Identify the blood parasite species.
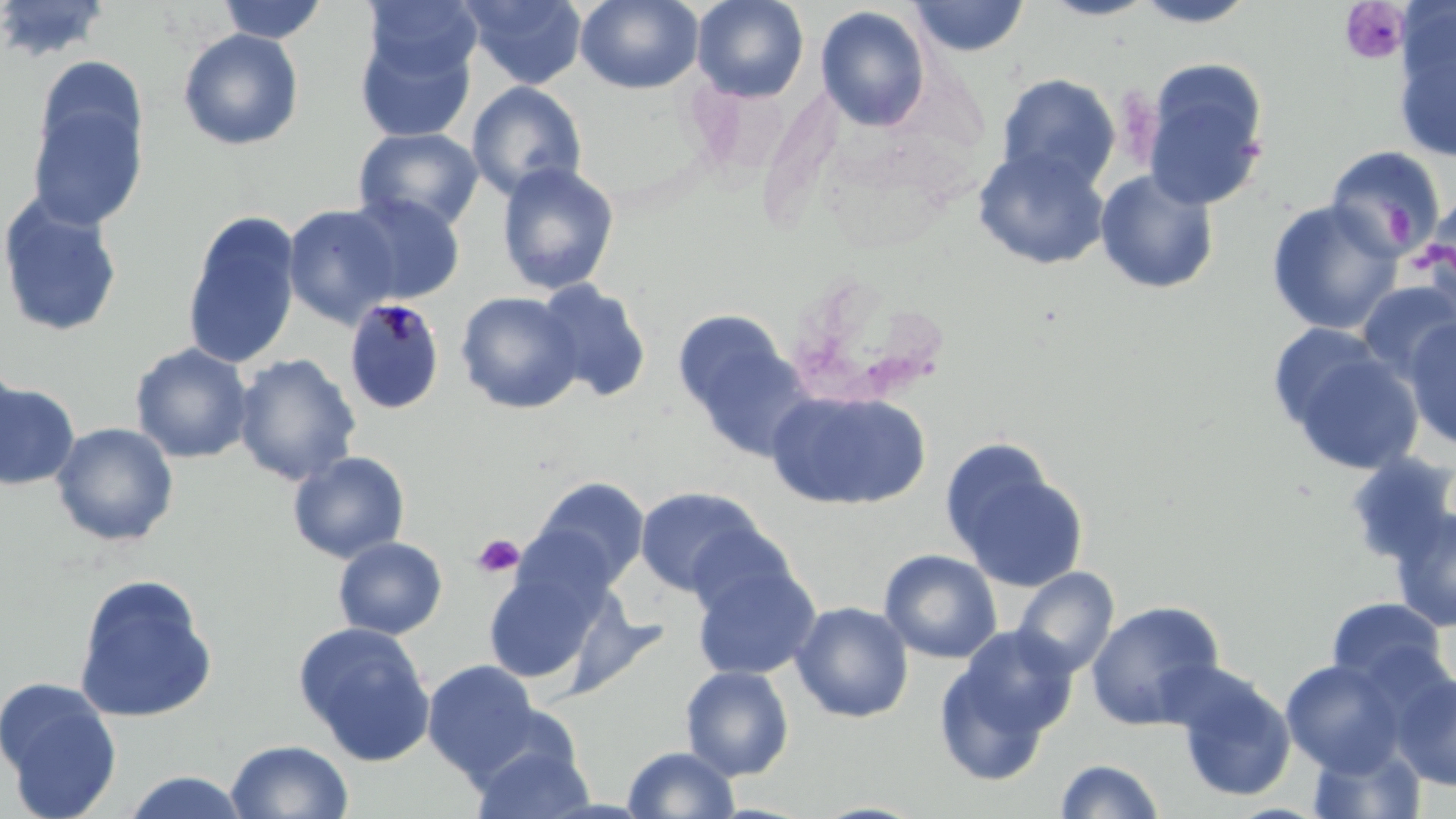
Plasmodium malariae.

Summary:
  - Coordinate format: approximate bounding boxes as (x1, y1, x2, y2) in pixels
  - Uninfected red blood cell locations: (0, 0, 112, 64), (217, 0, 328, 44), (461, 0, 587, 90), (575, 0, 703, 94), (692, 0, 810, 102), (1039, 0, 1158, 21), (1129, 0, 1263, 28), (363, 1, 482, 85), (909, 1, 1029, 57), (815, 5, 931, 132), (1390, 9, 1456, 163), (353, 20, 478, 143), (177, 28, 304, 151), (34, 55, 149, 168), (1141, 58, 1272, 211), (996, 73, 1121, 193), (466, 81, 587, 202), (27, 96, 147, 231), (353, 127, 483, 233), (973, 146, 1110, 270), (1324, 146, 1445, 261), (496, 161, 620, 296), (1095, 168, 1220, 295), (0, 193, 124, 338), (343, 193, 466, 306), (1422, 193, 1456, 288), (1265, 199, 1404, 335), (283, 204, 401, 328), (181, 211, 302, 369), (533, 279, 652, 402), (1356, 280, 1456, 383), (455, 291, 584, 414), (673, 311, 811, 460), (1403, 315, 1456, 452), (1265, 320, 1392, 437), (1282, 342, 1424, 475), (130, 343, 254, 464), (233, 353, 362, 486), (0, 358, 24, 479), (0, 380, 81, 491), (767, 389, 930, 510), (51, 422, 179, 546), (940, 441, 1089, 594), (287, 451, 411, 564), (1340, 451, 1456, 568), (526, 476, 650, 593), (635, 486, 766, 597), (1389, 506, 1456, 633), (332, 536, 448, 639), (879, 549, 1003, 664), (482, 555, 615, 685), (692, 560, 820, 681), (1011, 566, 1119, 679), (72, 573, 218, 723), (1325, 597, 1449, 691), (1085, 600, 1225, 730), (791, 601, 914, 723), (293, 620, 435, 766), (935, 644, 1060, 786), (1281, 659, 1406, 775), (422, 660, 540, 778), (680, 665, 795, 781), (1393, 671, 1456, 791), (1173, 672, 1296, 803), (0, 676, 123, 818), (469, 736, 594, 819), (225, 739, 354, 818), (1306, 741, 1428, 819), (622, 746, 740, 818), (1053, 758, 1167, 818), (120, 770, 252, 818)
  - Plasmodium malariae-infected red blood cell locations: (342, 297, 446, 415)
  - Platelet locations: (1338, 2, 1411, 67), (471, 533, 525, 579)
  - Image size: 1456×819 pixels
  - Modality: optical microscopy
  - Magnification: 1000x
  - Preparation: thin blood smear
  - Field of view: one of a larger specimen
  - Stain: May-Grünwald-Giemsa